Describe the morphology of the red blood cells.
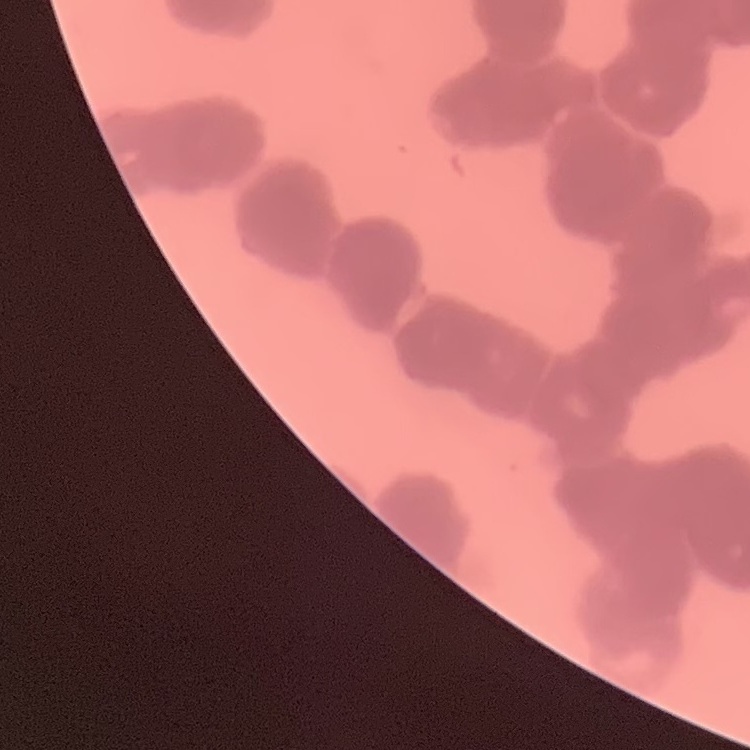
Rouleaux formation.

One tile cut from a larger photomicrograph. Stained with either Field's or Giemsa. Thin peripheral smear.